Identify the cell.
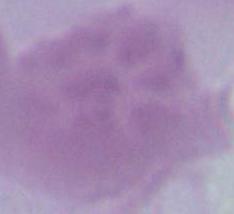

An erythrocyte.

Summary:
  - Magnification: 1000x
  - Modality: photomicrograph